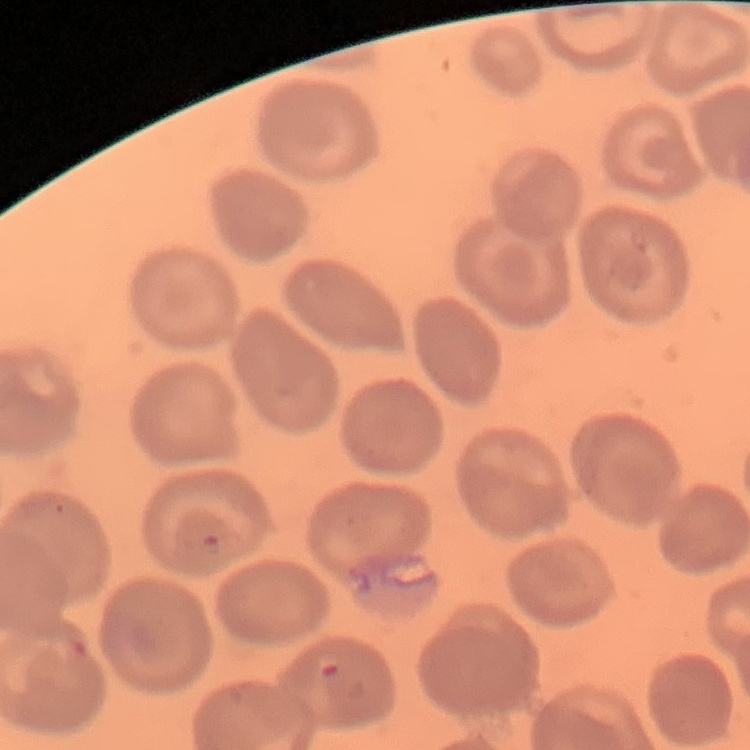

The red blood cells show no rouleaux formation. Field's or Giemsa stain. One tile cut from a larger photomicrograph. Thin blood smear.